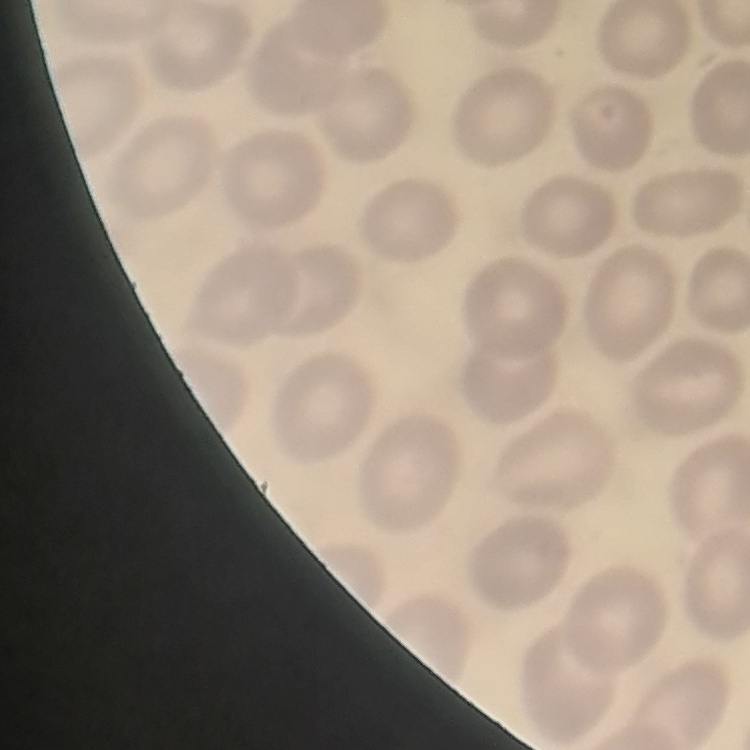
{
  "erythrocyte_morphology": "no rouleaux formation",
  "image_type": "square crop of a larger photomicrograph",
  "stain": "Field's or Giemsa",
  "preparation": "thin blood film"
}